Outline each blood parasite and name the species.
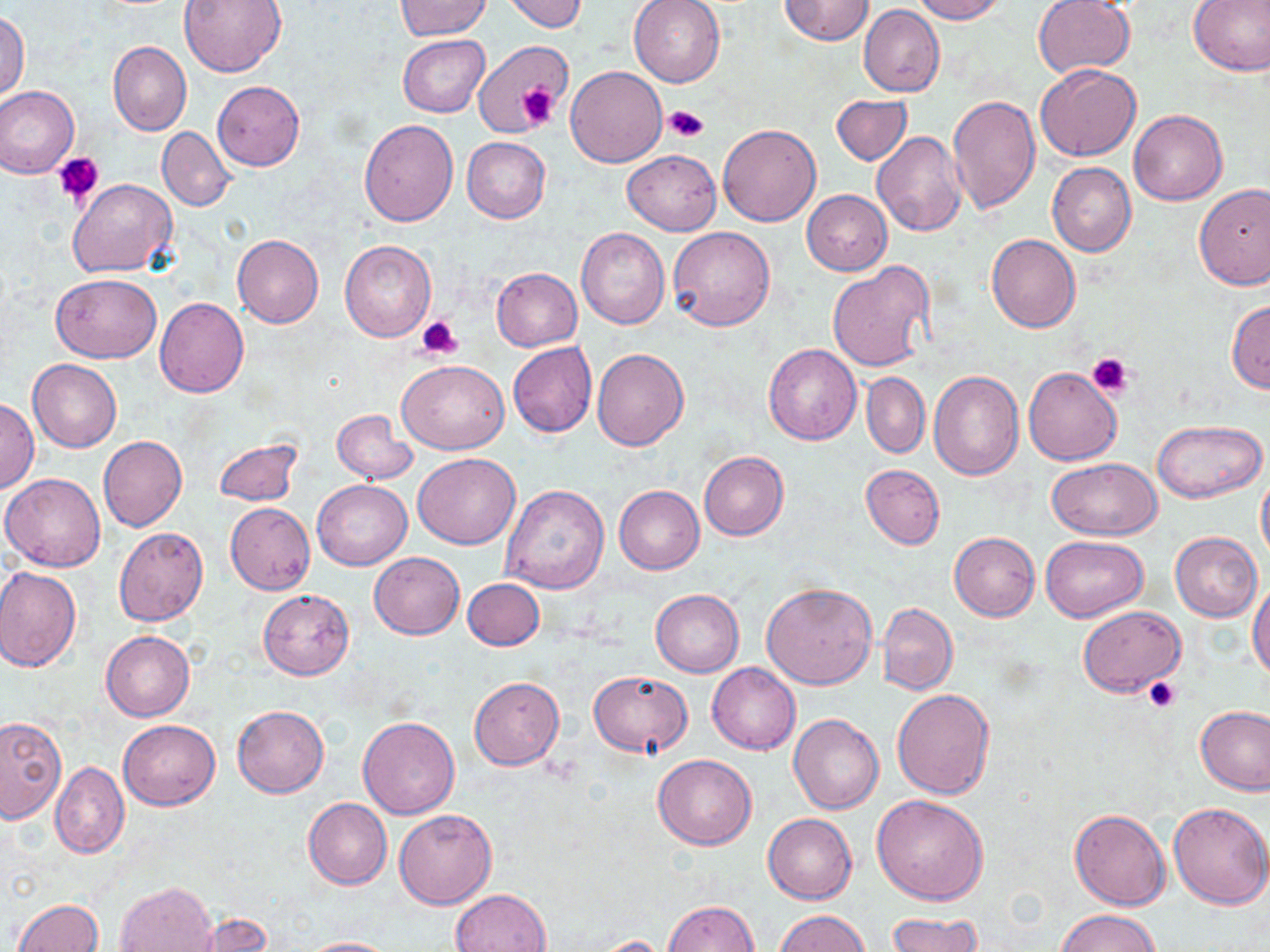
No blood parasites seen.

Approximate bounding boxes as (x1, y1, x2, y2) in pixels. Platelet locations: (514, 85, 558, 127), (664, 105, 708, 142), (53, 152, 105, 205), (417, 315, 463, 361), (1088, 353, 1131, 396), (1145, 676, 1180, 712). Uninfected red blood cell locations: (177, 0, 286, 77), (501, 0, 589, 33), (628, 0, 725, 87), (779, 0, 874, 45), (910, 0, 1007, 23), (1033, 0, 1136, 78), (1188, 0, 1270, 76), (394, 1, 491, 40), (859, 4, 944, 98), (0, 11, 29, 101), (398, 35, 488, 117), (474, 40, 571, 136), (108, 42, 192, 136), (1036, 64, 1141, 162), (566, 66, 666, 166), (213, 81, 304, 171), (0, 86, 79, 179), (946, 93, 1040, 214), (831, 94, 912, 165), (1130, 109, 1227, 205), (359, 118, 458, 225), (718, 123, 821, 227), (156, 127, 235, 211), (871, 130, 967, 237), (461, 137, 551, 223), (622, 149, 721, 235), (1048, 163, 1136, 257), (68, 177, 177, 277), (1194, 183, 1270, 290), (802, 190, 892, 275), (668, 226, 776, 330), (577, 228, 670, 329), (232, 234, 324, 328), (986, 234, 1081, 333), (340, 240, 436, 342), (827, 260, 936, 374), (491, 268, 582, 351), (50, 273, 161, 362), (155, 297, 248, 397), (1227, 300, 1270, 392), (508, 343, 596, 437), (763, 343, 862, 445), (592, 348, 688, 450), (28, 359, 121, 452), (397, 360, 508, 454), (1023, 366, 1122, 466), (928, 370, 1024, 479), (861, 373, 930, 459), (1, 398, 40, 492), (331, 409, 417, 485), (1152, 418, 1267, 502), (98, 435, 189, 532), (213, 438, 305, 507), (698, 451, 788, 540), (413, 453, 519, 549), (1045, 458, 1161, 541), (860, 464, 945, 548), (1256, 470, 1270, 569), (1, 472, 106, 572), (311, 480, 412, 571), (501, 484, 609, 593), (613, 485, 704, 574), (225, 503, 315, 595), (114, 526, 209, 626), (949, 531, 1039, 620), (1170, 531, 1263, 622), (1041, 535, 1149, 621), (369, 552, 464, 639), (0, 566, 80, 672), (463, 578, 544, 650), (1249, 578, 1270, 683), (761, 584, 877, 690), (650, 588, 744, 677), (257, 590, 354, 679), (879, 603, 957, 695), (1077, 606, 1185, 695), (100, 631, 194, 722), (707, 662, 801, 754), (588, 671, 692, 757), (469, 676, 564, 769), (892, 688, 995, 798), (233, 705, 329, 797), (1196, 707, 1270, 795), (788, 714, 884, 815), (0, 715, 68, 825), (357, 715, 460, 819), (117, 719, 221, 810), (653, 753, 757, 850), (50, 762, 129, 858), (871, 794, 988, 905), (303, 798, 392, 890), (1168, 803, 1270, 909), (394, 809, 496, 909), (1069, 809, 1171, 911), (763, 813, 857, 904), (115, 881, 217, 952), (451, 888, 552, 951), (12, 896, 104, 952), (663, 900, 759, 952), (774, 909, 869, 951), (1057, 909, 1160, 952), (886, 910, 981, 952), (187, 913, 272, 951), (585, 935, 672, 951), (297, 936, 395, 952). Slide-level diagnosis: no evidence of blood parasites. Captured at 1000x magnification. One field of a larger specimen. Image is 1270×952 pixels. May-Grünwald-Giemsa-stained preparation. Optical microscopy. Thin blood film.